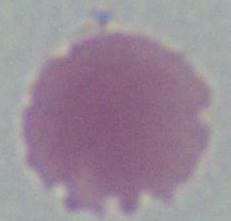
Summary:
  - Modality: photomicrograph
  - Identification: red blood cell
  - Magnification: 1000x